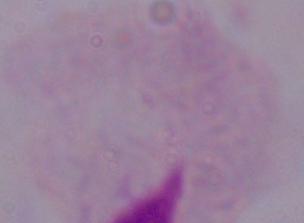

Photomicrograph. A trichomonad is shown. 1000x magnification.